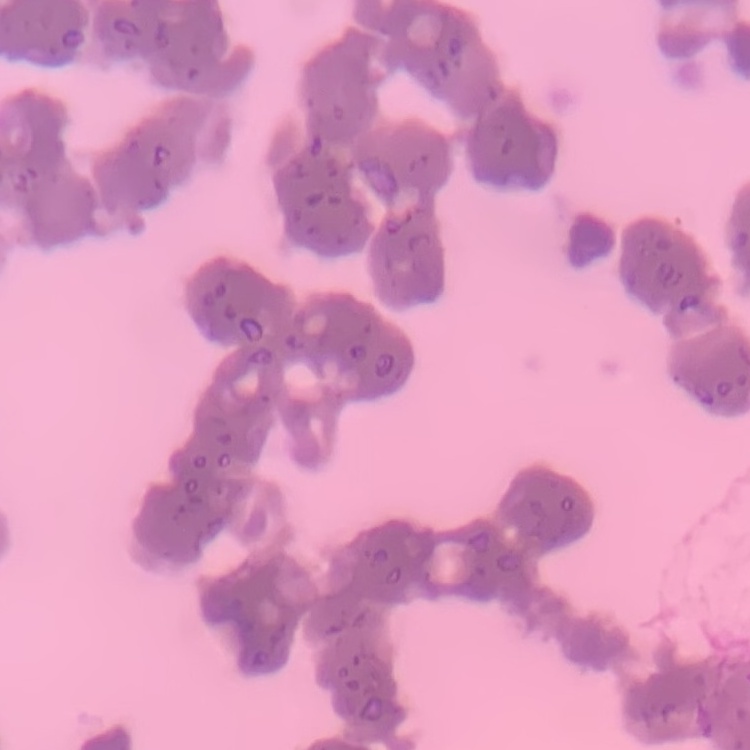 The red blood cells exhibit rouleaux formation. Thin peripheral smear. Square crop of a larger photomicrograph. Stained with either Field's or Giemsa.